Locate Plasmodium parasites and leukocytes.
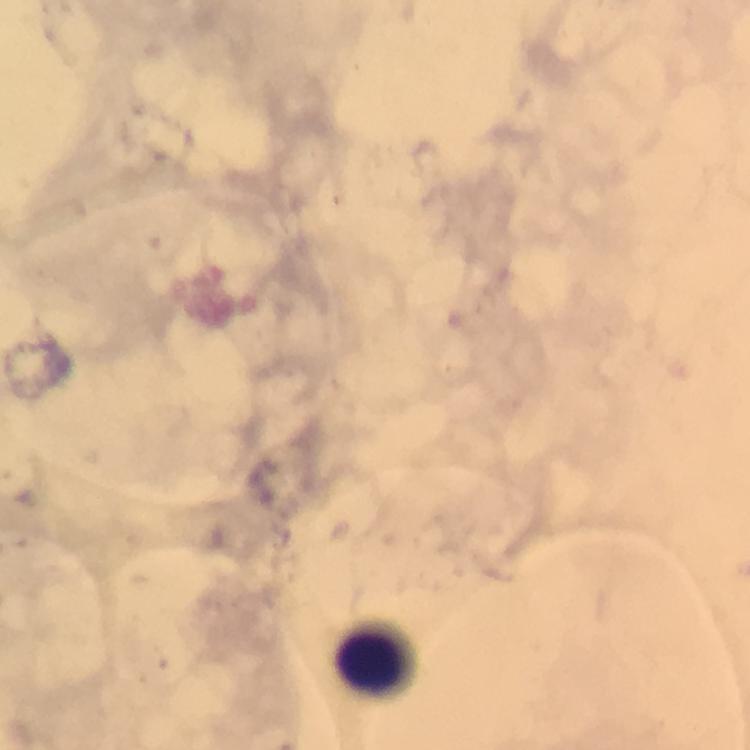

No Plasmodium parasites seen.
Approximate centers as {x, y} in pixels.
Leukocytes: {377, 655}.

stain = Giemsa
magnification = 100x
immersion oil = used
image size = 750×750 pixels
context = from a diagnostic examination for malaria
cropped from = a single field of view
preparation = thick blood film
capture = smartphone mounted on the microscope